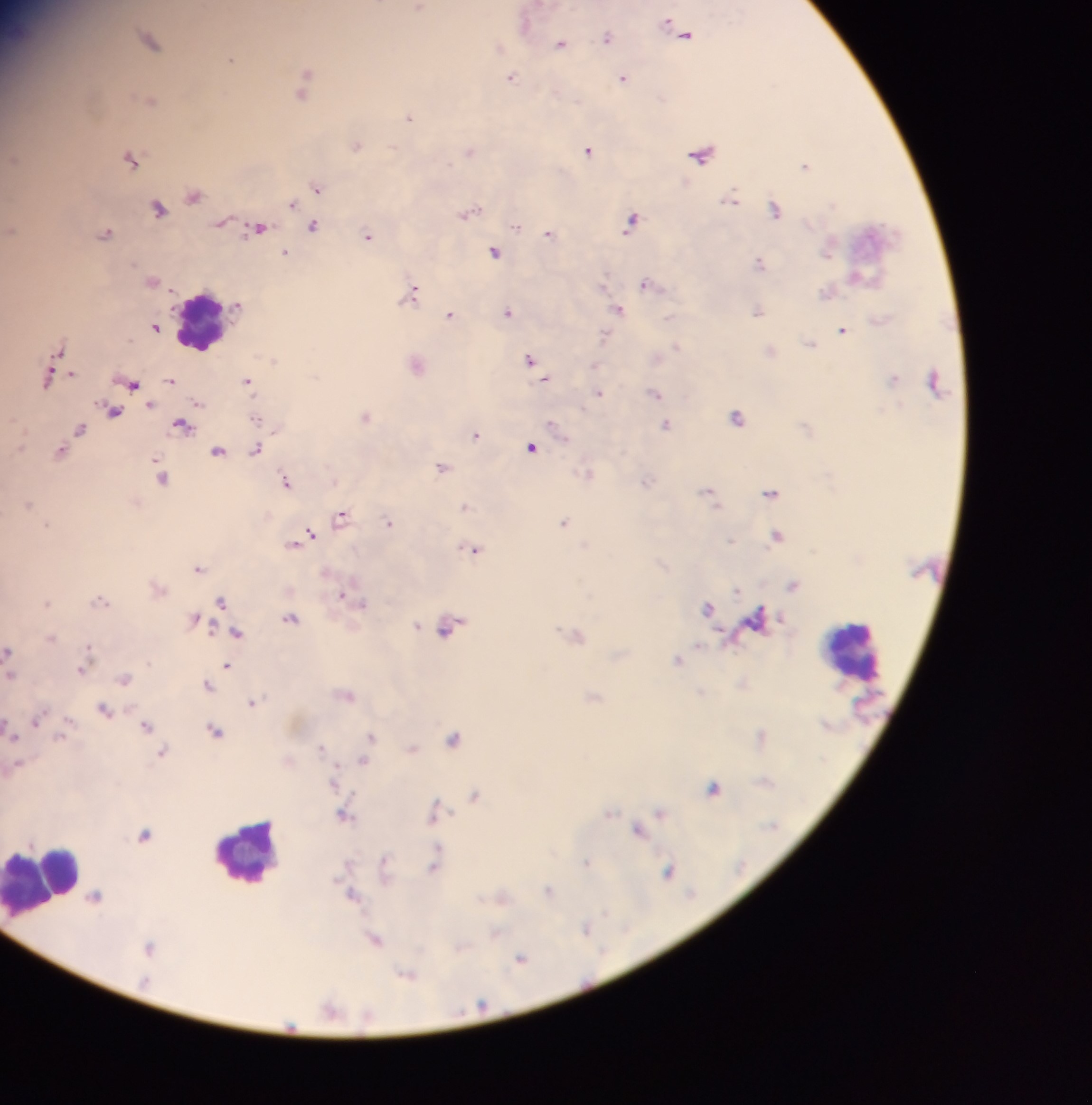
Approximate centers as x y in pixels. Malaria parasite locations: 418 8; 526 21; 674 28; 686 34; 607 36; 150 41; 560 43; 499 47; 231 59; 511 78; 624 78; 305 83; 149 99; 409 116; 356 145; 588 149; 469 151; 702 153; 131 158; 805 166; 316 188; 193 194; 730 199; 292 203; 158 208; 775 208; 468 212; 632 219; 222 221; 313 226; 516 226; 257 228; 10 230; 105 233; 550 233; 368 237; 829 248; 495 251; 284 253; 760 262; 151 281; 648 285; 412 292; 827 292; 619 309; 757 310; 507 311; 450 314; 878 320; 155 326; 843 329; 605 335; 809 343; 676 346; 59 349; 770 350; 656 357; 530 359; 272 360; 416 363; 594 365; 48 377; 894 378; 545 379; 170 380; 934 380; 247 381; 132 383; 599 393; 655 393; 198 403; 114 411; 365 416; 737 416; 667 424; 182 425; 555 427; 79 429; 476 433; 531 447; 255 449; 61 451; 217 451; 442 466; 588 473; 161 477; 287 481; 646 481; 710 492; 771 493; 27 504; 465 506; 341 516; 389 521; 564 521; 47 525; 311 533; 778 536; 302 538; 730 540; 293 544; 472 549; 198 568; 793 584; 158 587; 735 590; 344 596; 100 601; 221 601; 45 603; 708 608; 195 618; 757 618; 290 619; 416 625; 450 626; 237 633; 576 634; 50 638; 8 651; 678 660; 226 665; 83 668; 9 672; 124 678; 742 683; 207 685; 701 692; 346 694; 593 697; 253 701; 104 710; 35 719; 145 725; 215 730; 11 735; 371 736; 762 736; 453 738; 321 747; 411 748; 162 753; 363 761; 15 765; 333 782; 714 787; 474 795; 435 810; 661 811; 609 813; 344 814; 639 829; 144 836; 438 854; 587 862; 435 864; 384 866; 668 872; 549 891; 352 894; 94 896; 502 897; 586 928; 495 933; 375 938; 149 947; 521 958; 407 975; 330 1008. Leukocyte locations: 199 322; 852 652; 252 853; 39 881. Thick blood smear. Photographed through a microscope with a mobile-phone camera. One field of view. Image is 1092×1105 pixels. Collected in Ghana.